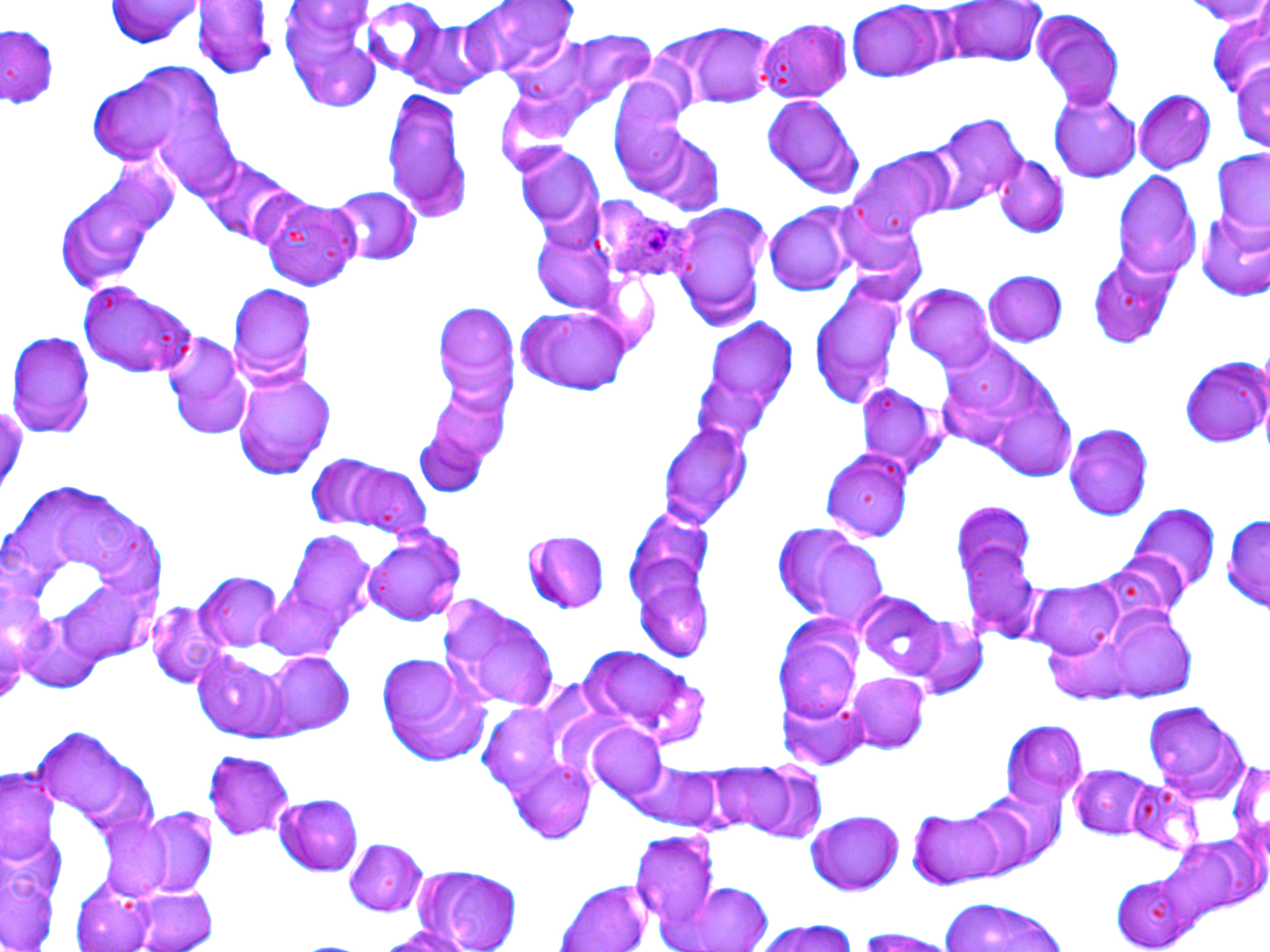

Approximate bounding boxes as (x1, y1, x2, y2) in pixels. White blood cell locations: (1, 475, 175, 694). Uninfected red blood cell locations: (108, 0, 198, 50), (197, 0, 273, 82), (466, 0, 576, 80), (936, 0, 1045, 69), (847, 3, 949, 84), (278, 5, 379, 108), (1030, 11, 1124, 111), (1205, 14, 1269, 98), (760, 20, 850, 103), (404, 22, 499, 98), (660, 26, 777, 109), (0, 28, 60, 105), (507, 29, 659, 129), (1228, 58, 1270, 152), (86, 69, 216, 164), (608, 79, 705, 198), (1134, 89, 1215, 172), (383, 91, 467, 219), (1050, 92, 1143, 182), (763, 97, 866, 199), (157, 115, 243, 202), (921, 115, 1025, 217), (641, 131, 726, 216), (516, 145, 607, 239), (1209, 151, 1269, 244), (199, 152, 294, 245), (852, 152, 950, 238), (992, 157, 1070, 238), (1112, 173, 1199, 284), (53, 178, 171, 292), (328, 186, 422, 265), (835, 194, 929, 287), (261, 196, 362, 293), (764, 204, 859, 297), (670, 206, 771, 329), (1195, 216, 1270, 299), (531, 226, 618, 315), (983, 270, 1068, 346), (807, 281, 911, 408), (77, 284, 198, 379), (227, 284, 318, 391), (903, 284, 999, 371), (517, 303, 638, 397), (699, 321, 801, 440), (7, 328, 97, 436), (164, 335, 257, 440), (941, 338, 1075, 480), (1181, 354, 1269, 450), (231, 369, 339, 479), (855, 380, 943, 476), (657, 418, 755, 531), (1065, 422, 1152, 519), (821, 448, 913, 541), (304, 452, 434, 540), (1, 481, 177, 698), (1129, 503, 1222, 596), (955, 520, 1044, 642), (770, 522, 892, 631), (516, 527, 614, 617), (363, 530, 467, 625), (1103, 547, 1190, 631), (195, 573, 286, 652), (633, 573, 715, 664), (1029, 579, 1127, 657), (857, 592, 952, 678), (147, 598, 232, 690), (444, 598, 562, 711), (1089, 604, 1199, 701), (776, 615, 868, 725), (908, 616, 988, 699), (579, 647, 704, 741), (375, 651, 495, 767), (184, 652, 305, 742), (262, 652, 359, 737), (846, 673, 929, 757), (1142, 703, 1250, 808), (1002, 720, 1088, 806), (587, 723, 667, 803), (204, 748, 297, 843), (1228, 751, 1270, 855), (504, 760, 594, 844), (720, 761, 826, 842), (624, 764, 726, 830), (1070, 764, 1159, 841), (2, 773, 60, 863), (1128, 777, 1204, 853), (942, 791, 1061, 881), (275, 795, 367, 875), (117, 807, 217, 894), (908, 807, 1016, 889), (804, 810, 906, 895), (1172, 833, 1265, 919), (632, 834, 719, 923), (344, 837, 428, 917), (0, 840, 64, 951), (411, 867, 524, 949), (1112, 874, 1194, 947), (70, 876, 161, 949), (558, 881, 651, 951), (673, 883, 775, 952), (938, 898, 1079, 952), (757, 920, 862, 952), (379, 925, 470, 951), (852, 928, 954, 950). Plasmodium ovale-infected red blood cell locations: (595, 196, 682, 284). Slide-level diagnosis: Plasmodium ovale. Thin blood film. Image is 1270×952 pixels. Captured at 1000x magnification. Optical microscopy. Single field of view. May-Grünwald-Giemsa stain.